Locate every Babesia divergens-infected red blood cell.
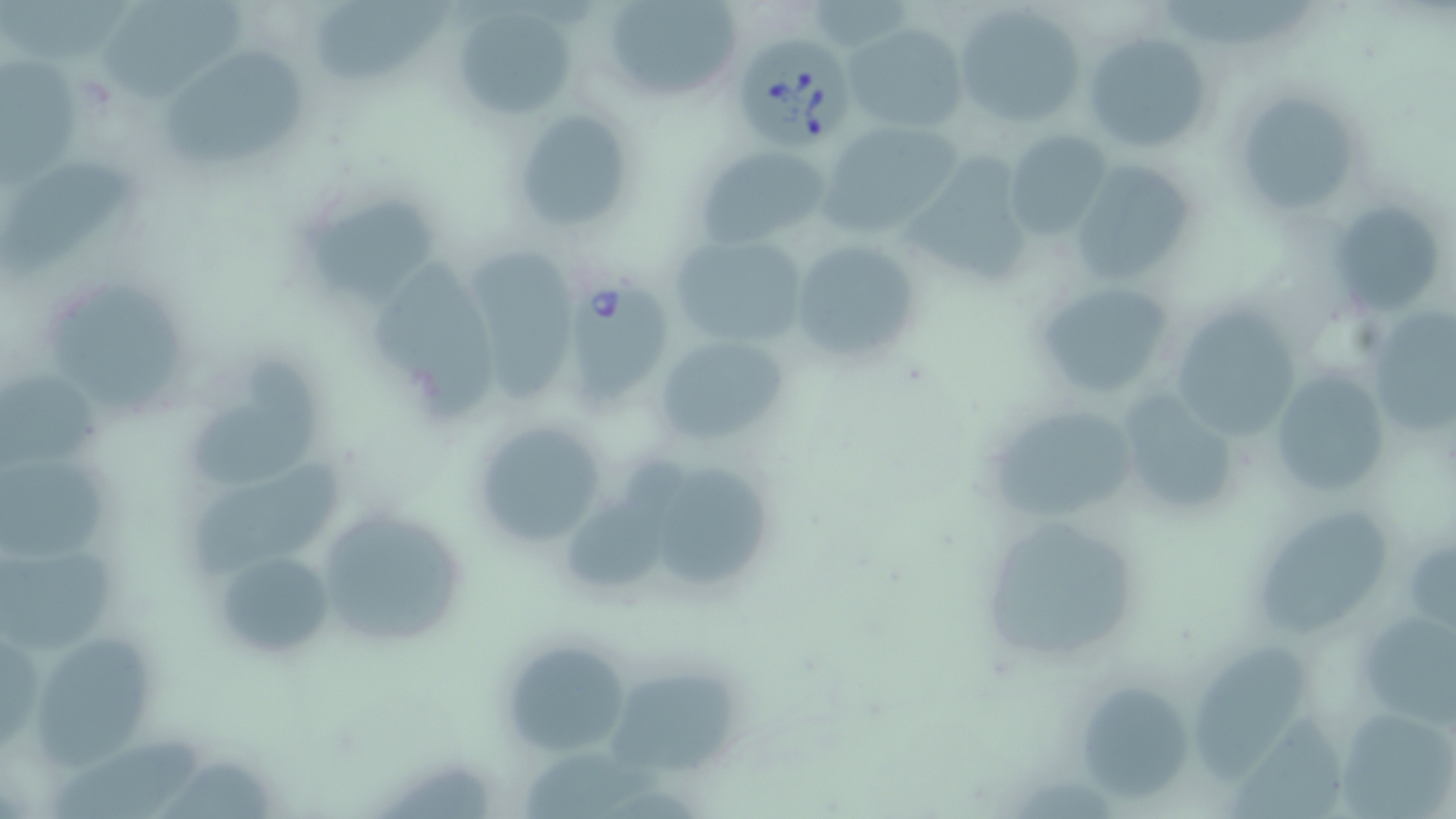
Approximate bounding boxes as [x1, y1, x2, y2] in pixels.
Babesia divergens-infected red blood cells: [729, 36, 852, 149], [565, 279, 672, 411].

Uninfected red blood cell locations: [604, 0, 741, 102], [94, 1, 253, 105], [314, 2, 458, 86], [954, 3, 1087, 128], [458, 12, 578, 119], [845, 23, 968, 133], [1084, 30, 1212, 156], [164, 48, 306, 168], [1, 52, 78, 193], [1231, 87, 1368, 222], [512, 108, 632, 231], [822, 120, 962, 233], [1005, 129, 1112, 239], [694, 144, 831, 248], [1, 158, 133, 275], [903, 159, 1038, 289], [1065, 159, 1200, 290], [304, 193, 446, 318], [1326, 198, 1450, 317], [669, 233, 810, 347], [790, 238, 922, 370], [472, 248, 582, 401], [362, 251, 491, 425], [37, 275, 197, 422], [1032, 280, 1181, 404], [1161, 301, 1303, 440], [1365, 306, 1456, 445], [649, 333, 790, 450], [194, 358, 327, 481], [1267, 367, 1396, 501], [0, 378, 114, 469], [1106, 386, 1249, 519], [981, 399, 1146, 524], [467, 414, 614, 549], [563, 453, 688, 587], [0, 456, 117, 559], [665, 468, 771, 590], [310, 503, 470, 651], [973, 508, 1148, 669], [1253, 513, 1393, 633], [208, 540, 343, 668], [0, 541, 114, 664], [1354, 605, 1456, 725], [497, 636, 634, 761], [39, 641, 154, 770], [1193, 645, 1310, 779], [613, 669, 741, 778], [1082, 685, 1186, 803], [1334, 704, 1456, 815], [1232, 709, 1349, 819], [56, 735, 202, 819]. Slide-level diagnosis: Babesia divergens. Captured at 1000x magnification. Image is 1456×819 pixels. Single field of view. May-Grünwald-Giemsa stain. Thin blood film. Optical microscopy.